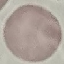
Summary:
  - Malaria status: uninfected
  - Image type: automatically extracted cell patch, resized to 64 × 64 pixels
  - Preparation: thin blood smear
  - Capture: smartphone camera at the microscope eyepiece
  - Stain: Giemsa